Identify the blood parasite species.
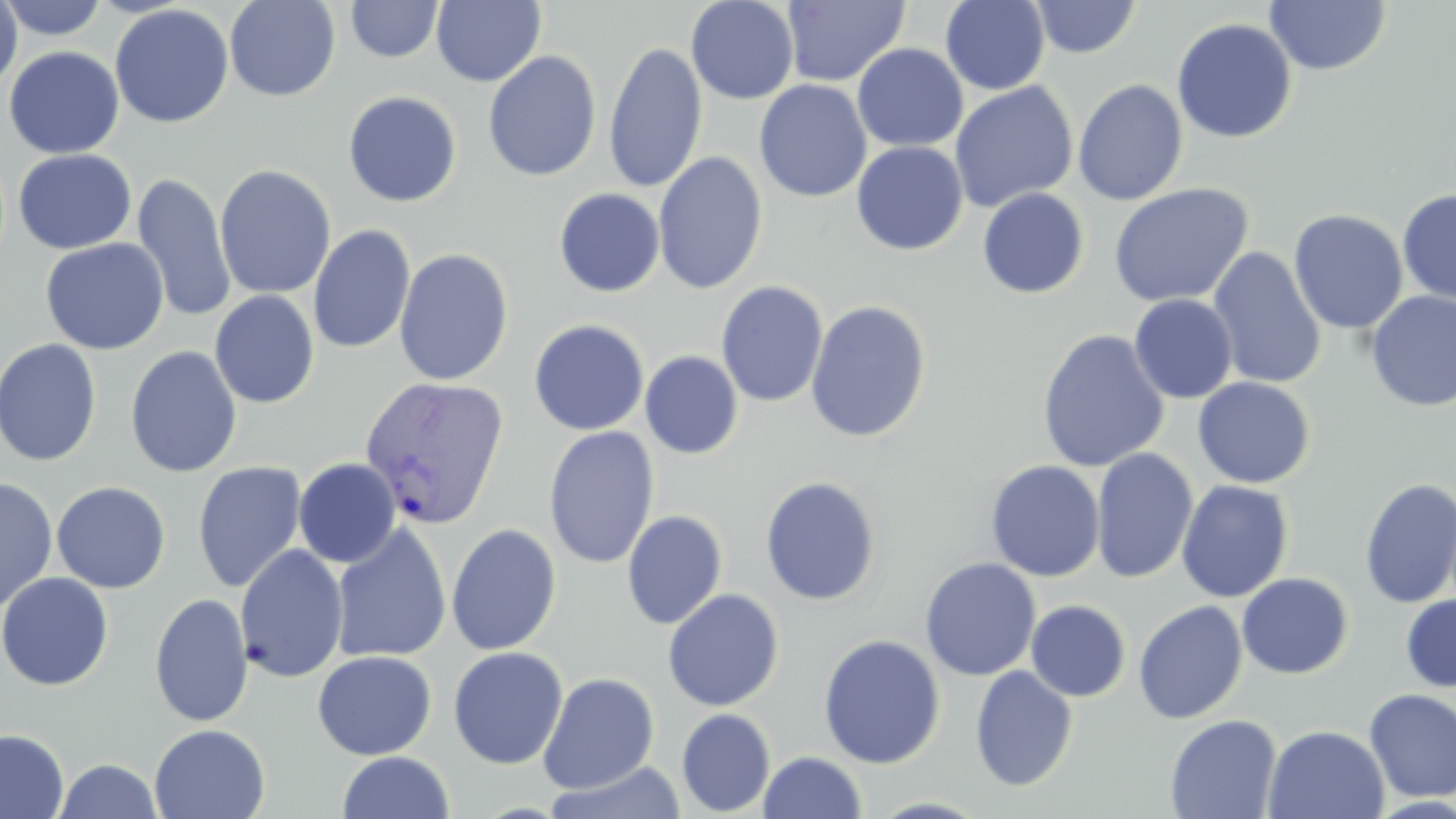

Plasmodium vivax.

preparation: thin blood film
plasmodium_vivax_infected_red_blood_cell_locations: 'approximate bounding boxes as [x1, y1, x2, y2] in pixels: [358, 375, 509, 531]'
uninfected_red_blood_cell_locations: 'approximate bounding boxes as [x1, y1, x2, y2] in pixels: [0, 0, 111, 41], [224, 0, 341, 101], [430, 0, 546, 87], [686, 0, 800, 105], [940, 0, 1051, 95], [345, 1, 444, 62], [782, 1, 909, 87], [1029, 1, 1142, 60], [1265, 1, 1391, 75], [0, 2, 23, 94], [109, 3, 234, 129], [1172, 18, 1297, 143], [603, 40, 707, 193], [852, 43, 968, 152], [3, 46, 124, 159], [482, 50, 602, 182], [754, 79, 872, 203], [1072, 79, 1189, 206], [949, 81, 1079, 213], [342, 90, 463, 207], [851, 141, 968, 256], [13, 149, 136, 254], [653, 151, 768, 295], [214, 164, 336, 299], [132, 173, 237, 323], [1108, 183, 1254, 308], [554, 188, 664, 297], [977, 188, 1090, 299], [1397, 189, 1456, 304], [1288, 209, 1409, 335], [308, 225, 415, 354], [39, 237, 170, 355], [1207, 247, 1326, 390], [393, 248, 514, 385], [716, 281, 829, 408], [209, 290, 320, 408], [1366, 291, 1456, 412], [1129, 294, 1238, 404], [805, 300, 932, 443], [529, 319, 649, 435], [1036, 329, 1170, 473], [0, 338, 103, 467], [125, 345, 243, 478], [640, 350, 743, 459], [1193, 377, 1315, 488], [543, 425, 660, 569], [1090, 448, 1198, 584], [293, 458, 401, 567], [985, 460, 1105, 582], [192, 461, 308, 593], [759, 476, 882, 606], [0, 477, 59, 613], [1359, 478, 1456, 609], [1176, 480, 1294, 602], [51, 481, 171, 593], [622, 510, 728, 629], [330, 522, 451, 662], [445, 523, 562, 656], [235, 543, 349, 683], [919, 557, 1041, 681], [0, 571, 114, 691], [1237, 572, 1354, 679], [662, 588, 785, 711], [149, 593, 253, 728], [1400, 593, 1456, 692], [1025, 600, 1131, 702], [1133, 600, 1248, 724], [817, 633, 945, 769], [448, 646, 568, 770], [312, 650, 437, 760], [970, 665, 1078, 792], [538, 672, 660, 793], [1363, 688, 1456, 803], [676, 708, 776, 817], [1164, 714, 1281, 818], [150, 723, 270, 819], [1263, 725, 1390, 819], [0, 728, 69, 819], [337, 751, 455, 819], [758, 751, 868, 818], [52, 758, 165, 818], [544, 760, 687, 819]'
image_size: 1456×819 pixels
magnification: 1000x
modality: optical microscopy
stain: May-Grünwald-Giemsa
field_of_view: single